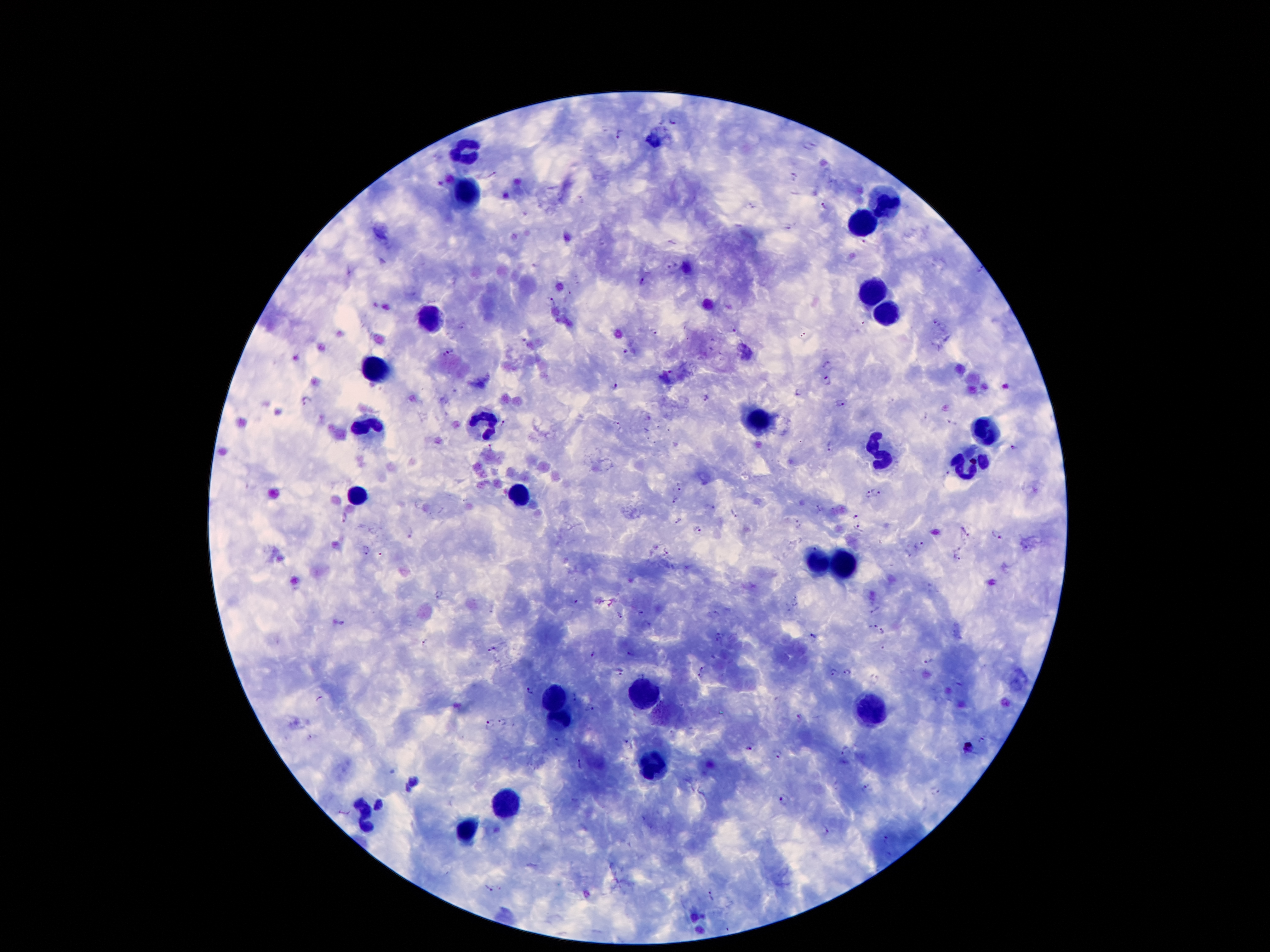

Approximate centers as [x, y] in pixels. Leukocyte locations: [655, 140], [465, 153], [469, 191], [884, 202], [863, 223], [868, 291], [889, 310], [432, 319], [376, 372], [486, 419], [751, 422], [369, 426], [985, 429], [878, 456], [969, 463], [519, 494], [353, 496], [815, 564], [842, 564], [644, 692], [554, 701], [875, 709], [561, 720], [658, 765], [507, 804], [367, 814], [467, 827]. Plasmodium parasite locations: [674, 118], [620, 132], [493, 173], [794, 175], [581, 197], [753, 203], [825, 205], [790, 227], [865, 240], [673, 265], [982, 268], [643, 281], [550, 301], [863, 322], [937, 322], [462, 325], [653, 331], [735, 331], [450, 351], [625, 351], [828, 365], [671, 373], [828, 380], [612, 386], [797, 391], [707, 398], [307, 400], [840, 402], [926, 416], [504, 422], [618, 425], [830, 444], [491, 447], [1015, 447], [949, 473], [679, 488], [877, 491], [868, 494], [674, 499], [820, 509], [735, 514], [855, 515], [344, 518], [678, 520], [797, 524], [858, 528], [697, 531], [965, 532], [413, 534], [996, 534], [918, 543], [667, 551], [366, 552], [956, 558], [440, 595], [576, 599], [875, 610], [641, 612], [618, 615], [342, 621], [648, 625], [872, 625], [884, 633], [722, 634], [814, 634], [424, 641], [883, 645], [492, 650], [594, 654], [631, 654], [928, 660], [704, 668], [834, 671], [848, 672], [621, 674], [700, 677], [531, 690], [575, 696], [591, 706], [800, 716], [490, 723], [503, 723], [982, 739], [558, 743], [626, 743], [967, 749], [750, 750], [846, 751], [779, 754], [579, 763], [414, 783], [866, 786], [936, 789], [784, 800], [379, 805], [826, 831], [887, 839], [488, 887], [712, 897]. Thick blood film. Smartphone photograph taken through the microscope eyepiece. Single field of view. Patient malaria status: infected with Plasmodium falciparum. Giemsa-stained preparation. 100x magnification. Image is 1270×952 pixels.